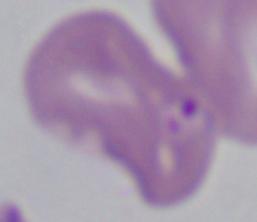
Micrograph. A Babesia parasite is seen. 1000x magnification.